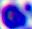
magnification = 400x
identification = leukocyte
modality = photomicrograph